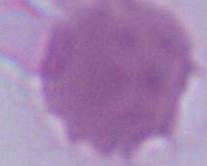
identification = erythrocyte
modality = micrograph
magnification = 1000x